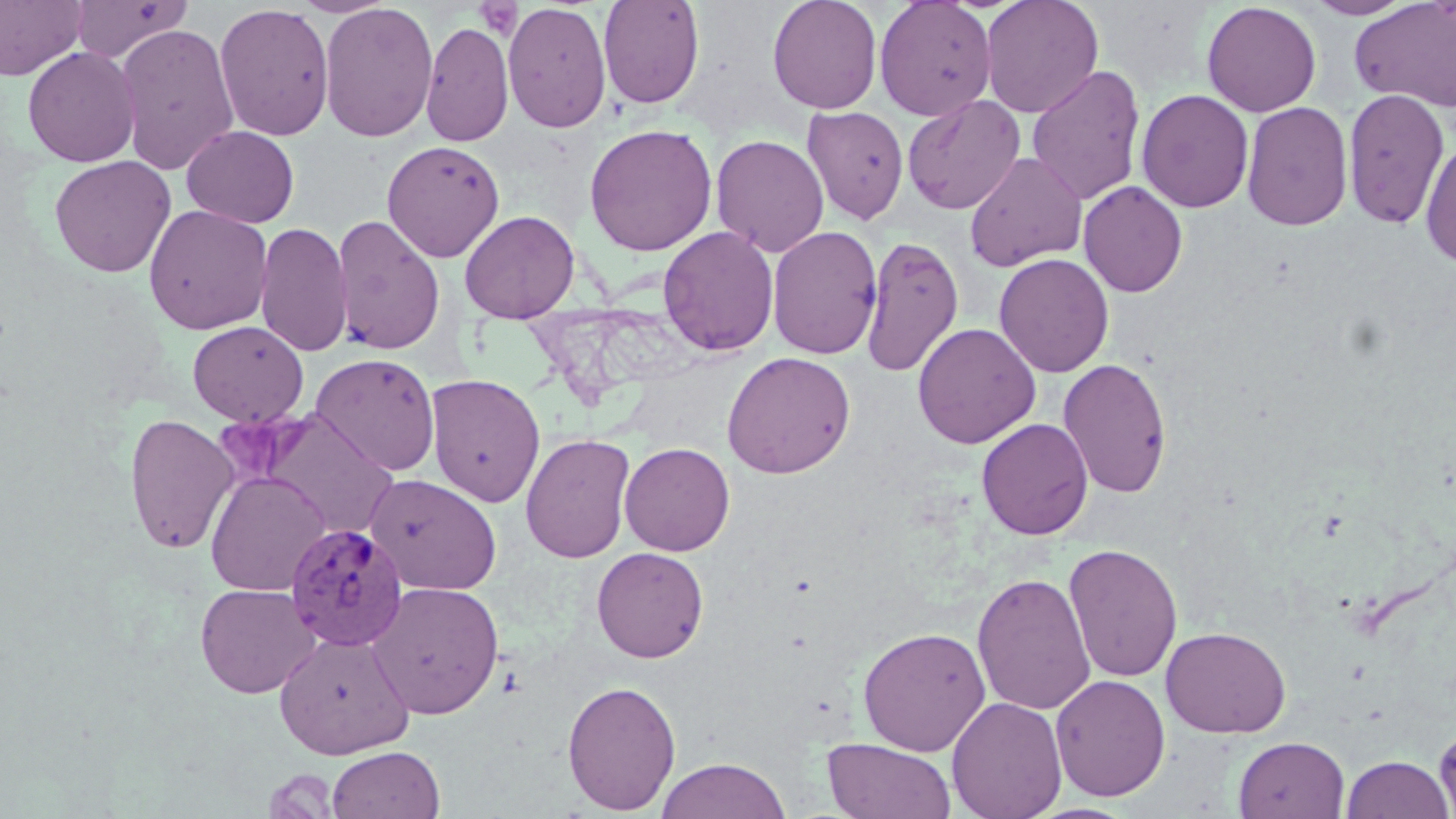

slide_level_diagnosis: Plasmodium vivax
preparation: thin blood film
modality: optical microscopy
platelet_locations: 'approximate bounding boxes as [x1, y1, x2, y2] in pixels: [472, 1, 523, 40]'
stain: May-Grünwald-Giemsa
uninfected_red_blood_cell_locations: 'approximate bounding boxes as [x1, y1, x2, y2] in pixels: [0, 0, 87, 80], [69, 0, 191, 63], [598, 0, 705, 109], [767, 0, 882, 113], [874, 0, 997, 120], [980, 0, 1104, 118], [1302, 0, 1418, 20], [1350, 0, 1456, 113], [502, 1, 612, 133], [1201, 1, 1321, 117], [214, 3, 335, 141], [318, 3, 439, 142], [420, 21, 514, 147], [114, 23, 239, 176], [22, 46, 140, 167], [1026, 65, 1146, 207], [1342, 88, 1450, 229], [1137, 89, 1254, 213], [902, 94, 1026, 215], [1241, 101, 1353, 232], [802, 106, 909, 225], [584, 123, 717, 256], [182, 125, 299, 228], [711, 134, 829, 258], [1419, 138, 1456, 268], [381, 140, 505, 262], [964, 151, 1087, 272], [49, 155, 176, 278], [1079, 181, 1187, 297], [143, 204, 273, 334], [460, 209, 580, 322], [331, 213, 445, 355], [255, 220, 353, 358], [767, 225, 883, 360], [658, 226, 779, 356], [861, 234, 964, 377], [993, 253, 1114, 377], [188, 321, 308, 426], [912, 322, 1040, 449], [721, 351, 857, 478], [310, 352, 441, 475], [1058, 357, 1173, 499], [425, 373, 546, 508], [259, 410, 400, 539], [124, 412, 240, 556], [976, 417, 1093, 540], [520, 433, 636, 563], [619, 442, 735, 556], [205, 470, 331, 596], [364, 473, 502, 594], [1063, 542, 1183, 683], [591, 547, 709, 663], [971, 572, 1096, 715], [367, 581, 504, 719], [195, 583, 320, 698], [857, 625, 991, 756], [1160, 626, 1291, 738], [274, 631, 415, 759], [1050, 674, 1171, 801], [562, 679, 682, 814], [946, 696, 1067, 819], [1435, 717, 1456, 817], [1233, 736, 1350, 819], [822, 737, 956, 819], [326, 745, 445, 819], [1340, 753, 1454, 819], [655, 756, 791, 819], [261, 768, 340, 819]'
image_size: 1456×819 pixels
field_of_view: one of a larger specimen
plasmodium_vivax_infected_red_blood_cell_locations: 'approximate bounding boxes as [x1, y1, x2, y2] in pixels: [284, 521, 410, 651]'
magnification: 1000x